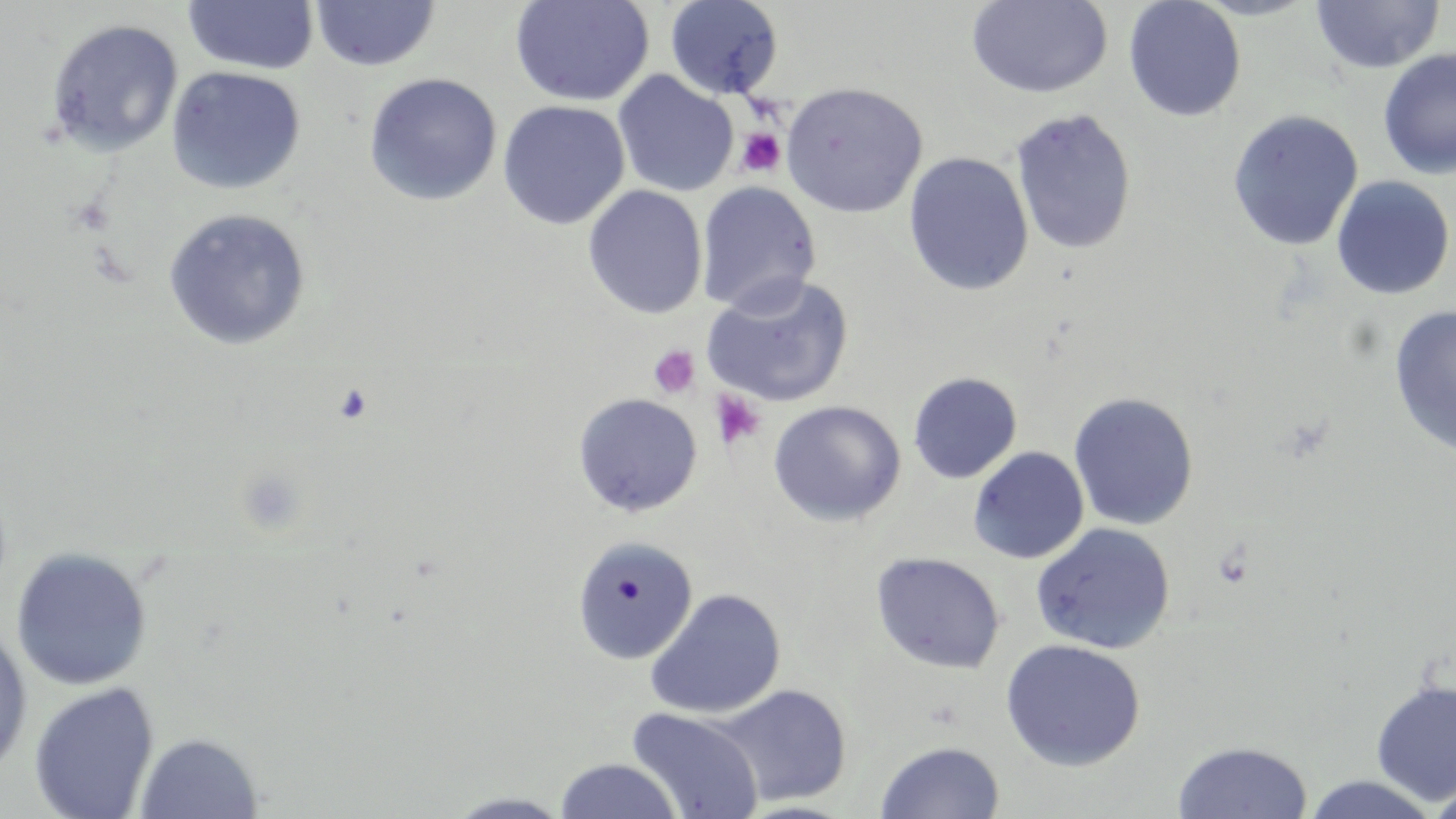
Summary:
  - Coordinate format: approximate bounding boxes as (x1, y1, x2, y2) in pixels
  - Uninfected red blood cell locations: (665, 0, 784, 99), (965, 0, 1113, 99), (1123, 0, 1247, 122), (182, 1, 320, 75), (310, 1, 440, 73), (509, 1, 655, 107), (1310, 1, 1445, 74), (44, 17, 184, 158), (1377, 48, 1456, 180), (166, 66, 306, 195), (612, 71, 739, 198), (363, 72, 503, 207), (780, 81, 928, 218), (497, 100, 630, 230), (1009, 108, 1137, 255), (1226, 109, 1363, 251), (903, 152, 1034, 296), (1331, 176, 1454, 300), (696, 181, 821, 316), (583, 185, 708, 320), (162, 207, 311, 351), (701, 275, 854, 408), (1388, 304, 1456, 459), (908, 372, 1022, 484), (1068, 391, 1199, 531), (572, 392, 703, 518), (767, 400, 906, 527), (968, 446, 1089, 565), (1031, 522, 1176, 655), (570, 535, 699, 665), (10, 547, 153, 692), (870, 551, 1005, 674), (645, 587, 786, 719), (0, 622, 33, 780), (1000, 638, 1146, 772), (1370, 677, 1456, 806), (27, 681, 161, 818), (712, 683, 852, 807), (626, 707, 764, 819), (133, 731, 264, 819), (875, 739, 1005, 819), (1172, 740, 1313, 818), (553, 757, 685, 819), (1301, 773, 1441, 818), (1426, 775, 1456, 819), (442, 791, 576, 818)
  - Platelet locations: (736, 128, 786, 178), (69, 194, 115, 238), (648, 346, 700, 400), (709, 389, 766, 450)
  - Slide-level diagnosis: negative for blood parasites
  - Modality: light microscopy
  - Magnification: 1000x
  - Image size: 1456×819 pixels
  - Preparation: thin blood smear
  - Field of view: one of a larger specimen
  - Stain: May-Grünwald-Giemsa